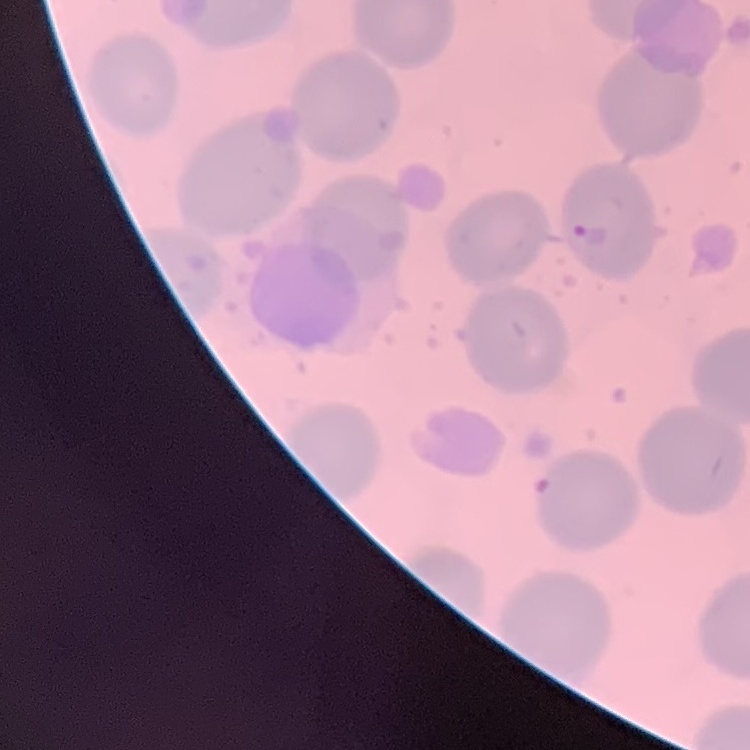

Summary:
  - Red blood cell morphology: no rouleaux formation
  - Preparation: thin peripheral smear
  - Image type: square crop of a larger photomicrograph
  - Stain: Field's or Giemsa